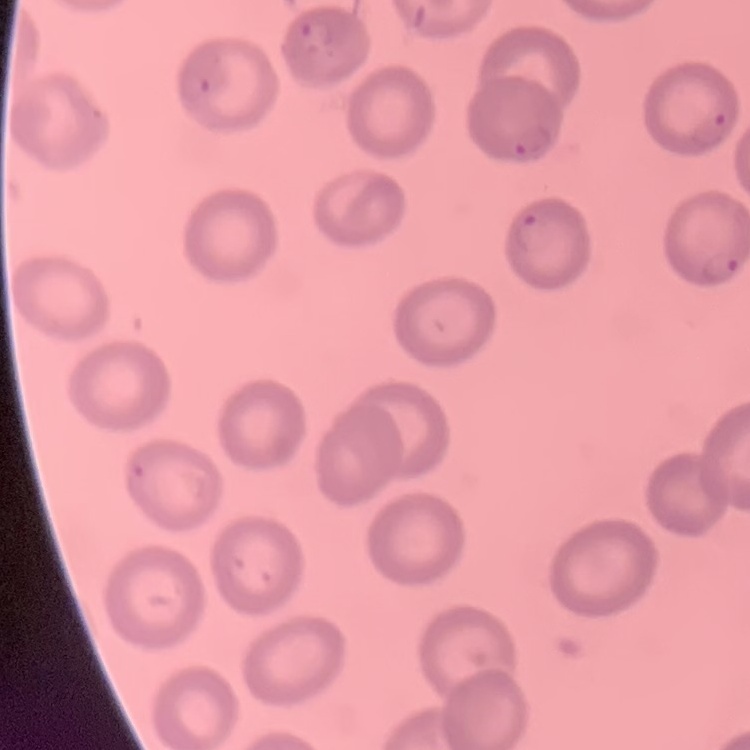
The erythrocytes exhibit no rouleaux formation. Stained with either Field's or Giemsa. Square crop of a larger photomicrograph. Thin blood smear.